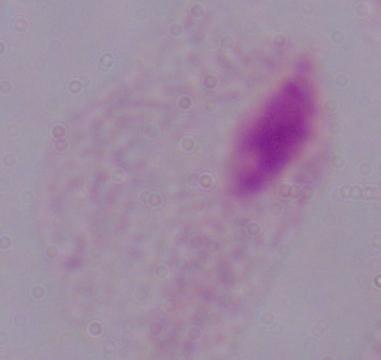
modality = photomicrograph
magnification = 1000x
identification = trichomonad